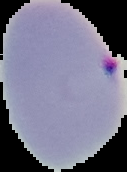

image type = segmented cell region with the area outside set to black
image size = 127×172 pixels
malaria status = parasitized
preparation = thin blood smear